Classify this cell by malaria status.
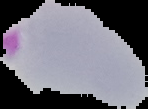
Parasitized.

Summary:
  - Image size: 148×109 pixels
  - Image type: cell region segmented out of the field of view; surrounding area masked to black
  - Preparation: thin blood smear